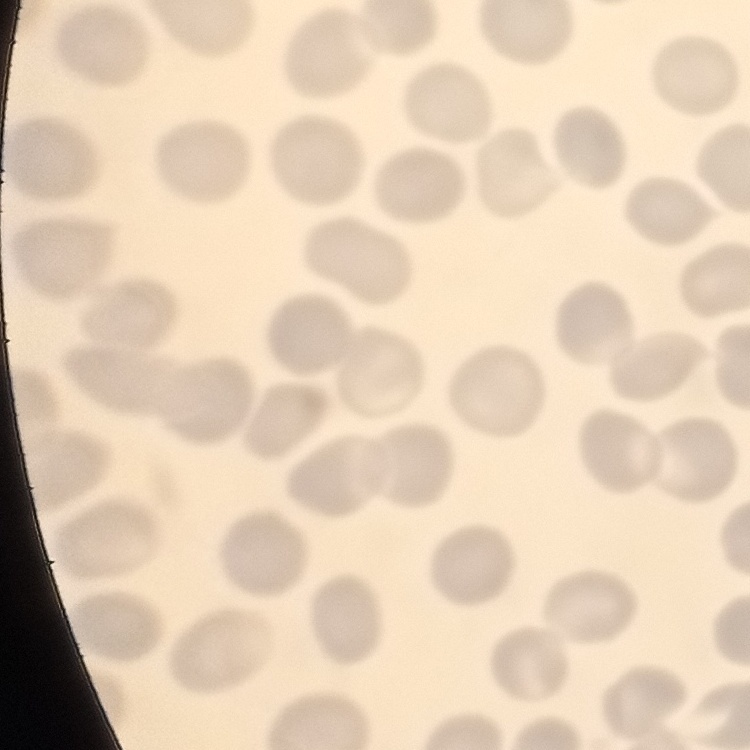

Summary:
  - Red blood cell morphology: no rouleaux formation
  - Preparation: thin blood film
  - Stain: Field's or Giemsa
  - Image type: square crop of a larger photomicrograph